Report the malaria status of this cell.
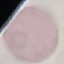

Uninfected.

Cell patch, automatically extracted from a larger field of view and resized to 64 × 64 pixels. Giemsa-stained preparation. Acquired by smartphone through the microscope eyepiece. Thin blood smear.